Assess this cell for malaria.
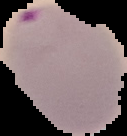
It is parasitized.

image size = 127×136 pixels
image type = segmented cell region with the area outside set to black
preparation = thin blood smear